Assess the morphology of the erythrocytes.
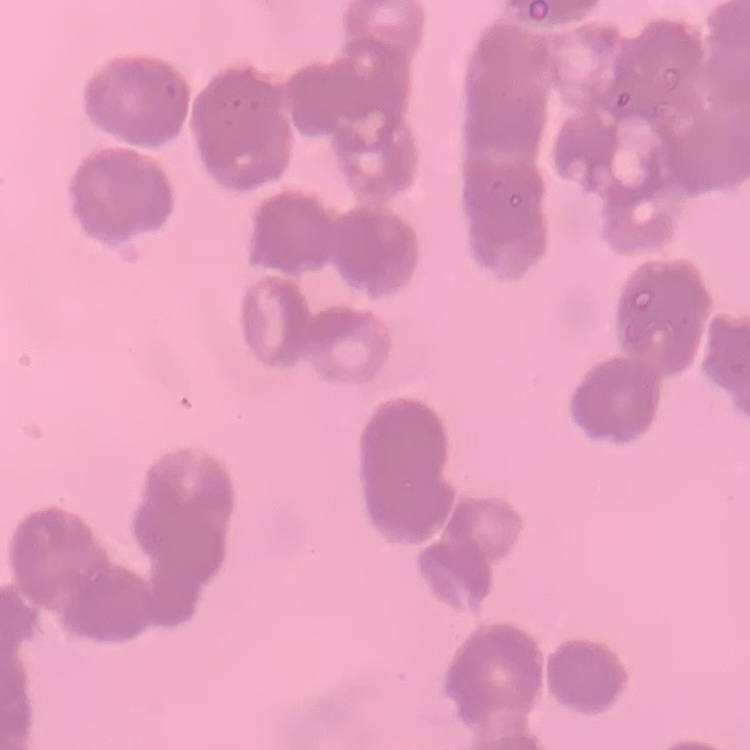

They show rouleaux formation.

Stained with either Field's or Giemsa. Thin blood film. One tile cut from a larger photomicrograph.